Report the malaria status of this cell.
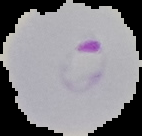
It is parasitized.

The area outside the segmented cell region is set to black. Image is 142×136 pixels. From a thin blood smear.